Give the extent of all uninfected red blood cells.
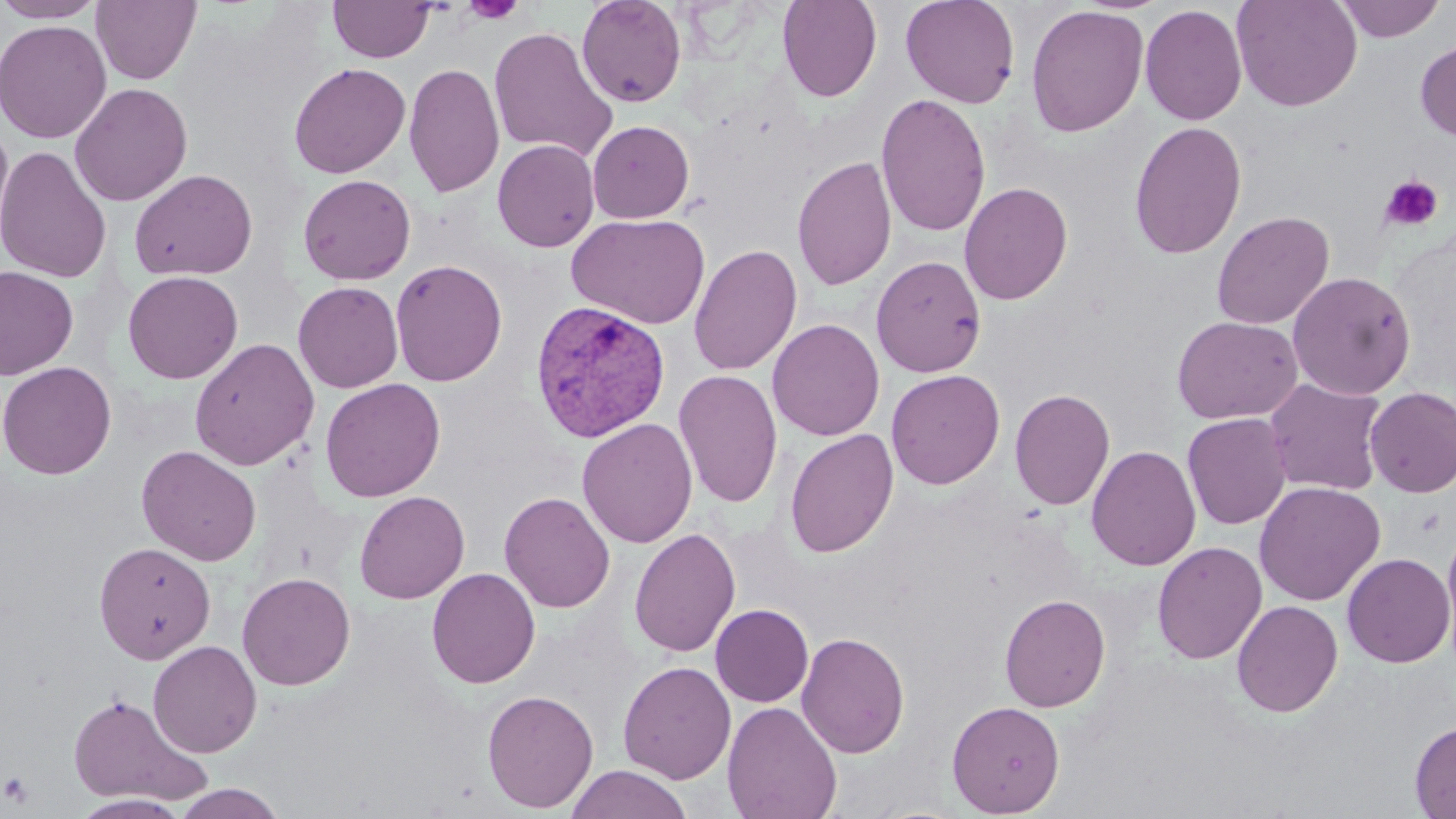
Approximate bounding boxes as (x1,y1)-(x2,y2) corner pairs in pixels.
Uninfected red blood cells: (0,0)-(107,23), (91,0)-(202,85), (328,0)-(435,63), (576,0)-(687,108), (777,0)-(882,102), (900,0)-(1020,108), (1231,0)-(1363,112), (1334,1)-(1445,42), (1025,4)-(1149,138), (1139,4)-(1247,125), (0,20)-(112,143), (488,26)-(618,164), (1415,38)-(1456,142), (288,62)-(411,179), (403,62)-(505,199), (69,82)-(193,207), (875,93)-(991,238), (587,120)-(695,223), (1129,120)-(1247,260), (0,124)-(15,250), (493,139)-(600,252), (0,145)-(112,284), (791,154)-(897,291), (130,168)-(258,281), (298,174)-(416,285), (959,181)-(1073,305), (1211,211)-(1334,330), (566,213)-(710,329), (689,243)-(802,376), (871,255)-(986,377), (390,258)-(507,387), (0,265)-(78,380), (122,270)-(243,384), (1287,270)-(1417,399), (293,281)-(403,393), (1171,315)-(1302,424), (767,318)-(885,441), (189,338)-(320,471), (1,361)-(117,480), (886,369)-(1005,489), (673,370)-(783,508), (320,378)-(445,502), (1264,378)-(1389,497), (1009,387)-(1115,511), (1364,387)-(1456,498), (1182,413)-(1291,530), (577,417)-(698,547), (783,428)-(899,558), (136,444)-(261,566), (1086,444)-(1201,571), (1254,481)-(1386,605), (355,491)-(469,604), (499,491)-(616,613), (1441,518)-(1456,657), (629,528)-(741,657), (94,541)-(216,663), (1151,541)-(1267,665), (1342,552)-(1455,668), (426,567)-(540,688), (236,571)-(356,691), (999,593)-(1110,712), (1231,599)-(1343,717), (711,604)-(813,707), (796,631)-(909,758), (147,640)-(262,758), (617,661)-(737,784), (481,689)-(599,813), (66,692)-(212,806), (946,700)-(1065,817), (722,701)-(843,819), (1410,720)-(1456,818), (565,764)-(693,819), (172,783)-(287,819), (71,794)-(191,818).

Summary:
  - Plasmodium vivax-infected red blood cell locations: (529,299)-(671,442)
  - Platelet locations: (461,0)-(526,25), (1379,175)-(1444,232), (1,771)-(35,807)
  - Slide-level diagnosis: Plasmodium vivax
  - Image size: 1456×819 pixels
  - Field of view: one of a larger specimen
  - Magnification: 1000x
  - Preparation: thin blood film
  - Stain: May-Grünwald-Giemsa
  - Modality: light microscopy